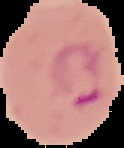

Summary:
  - Image type: segmented cell region on a black background
  - Image size: 124×148 pixels
  - Preparation: thin blood film
  - Result: Plasmodium parasites detected